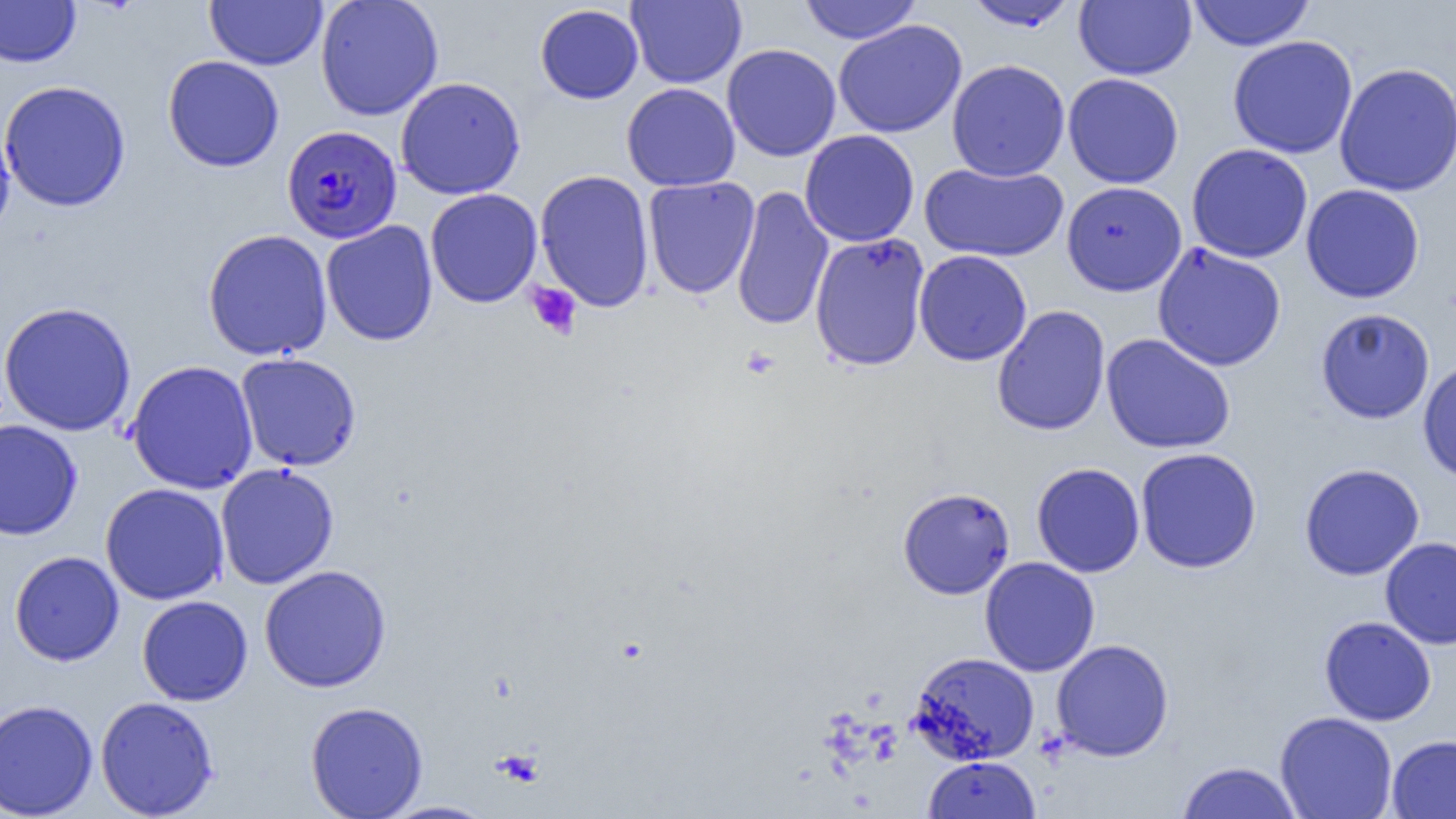 Approximate bounding boxes as (x1, y1, x2, y2) in pixels. Uninfected red blood cell locations: (204, 0, 328, 70), (315, 0, 444, 120), (626, 0, 747, 88), (1074, 0, 1196, 80), (1187, 0, 1316, 51), (0, 1, 81, 68), (797, 1, 923, 44), (964, 1, 1078, 31), (534, 3, 644, 104), (833, 19, 967, 138), (1227, 35, 1358, 159), (721, 43, 841, 161), (163, 55, 285, 172), (946, 59, 1071, 181), (1334, 62, 1456, 197), (1062, 73, 1184, 189), (395, 76, 526, 200), (0, 80, 132, 212), (622, 82, 740, 191), (0, 118, 16, 242), (799, 130, 919, 247), (1186, 143, 1313, 263), (919, 161, 1069, 262), (534, 169, 655, 312), (642, 177, 760, 299), (1061, 181, 1187, 296), (1300, 184, 1425, 304), (731, 186, 834, 331), (425, 188, 543, 308), (320, 220, 438, 347), (202, 229, 333, 361), (809, 232, 931, 372), (1151, 242, 1287, 371), (914, 249, 1032, 366), (0, 301, 137, 437), (992, 305, 1111, 436), (1315, 307, 1435, 424), (1101, 333, 1236, 454), (1118, 334, 1245, 571), (235, 353, 362, 471), (1417, 358, 1456, 484), (126, 360, 259, 495), (0, 419, 83, 540), (1135, 447, 1262, 573), (1031, 462, 1145, 578), (215, 463, 339, 589), (1299, 463, 1425, 581), (100, 482, 230, 605), (898, 487, 1015, 599), (1380, 536, 1456, 649), (9, 551, 124, 666), (979, 556, 1100, 677), (259, 564, 391, 692), (137, 595, 253, 706), (1319, 615, 1437, 726), (1051, 639, 1174, 761), (909, 651, 1040, 765), (95, 696, 219, 818), (0, 699, 98, 819), (305, 701, 429, 819), (1275, 711, 1398, 819), (1386, 734, 1456, 818), (922, 756, 1041, 819), (1176, 761, 1304, 818), (379, 800, 499, 818). Platelet locations: (526, 282, 583, 339), (493, 749, 544, 788). Plasmodium falciparum-infected red blood cell locations: (282, 124, 402, 244). Slide-level diagnosis: Plasmodium falciparum. Single field of view. Image is 1456×819 pixels. Light microscopy. 1000x magnification. Thin blood film.